Assess this cell for malaria.
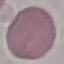

Uninfected.

Acquired by smartphone through the microscope eyepiece. Automatically extracted cell patch, resized to 64 × 64 pixels. Thin blood film. Giemsa stain.